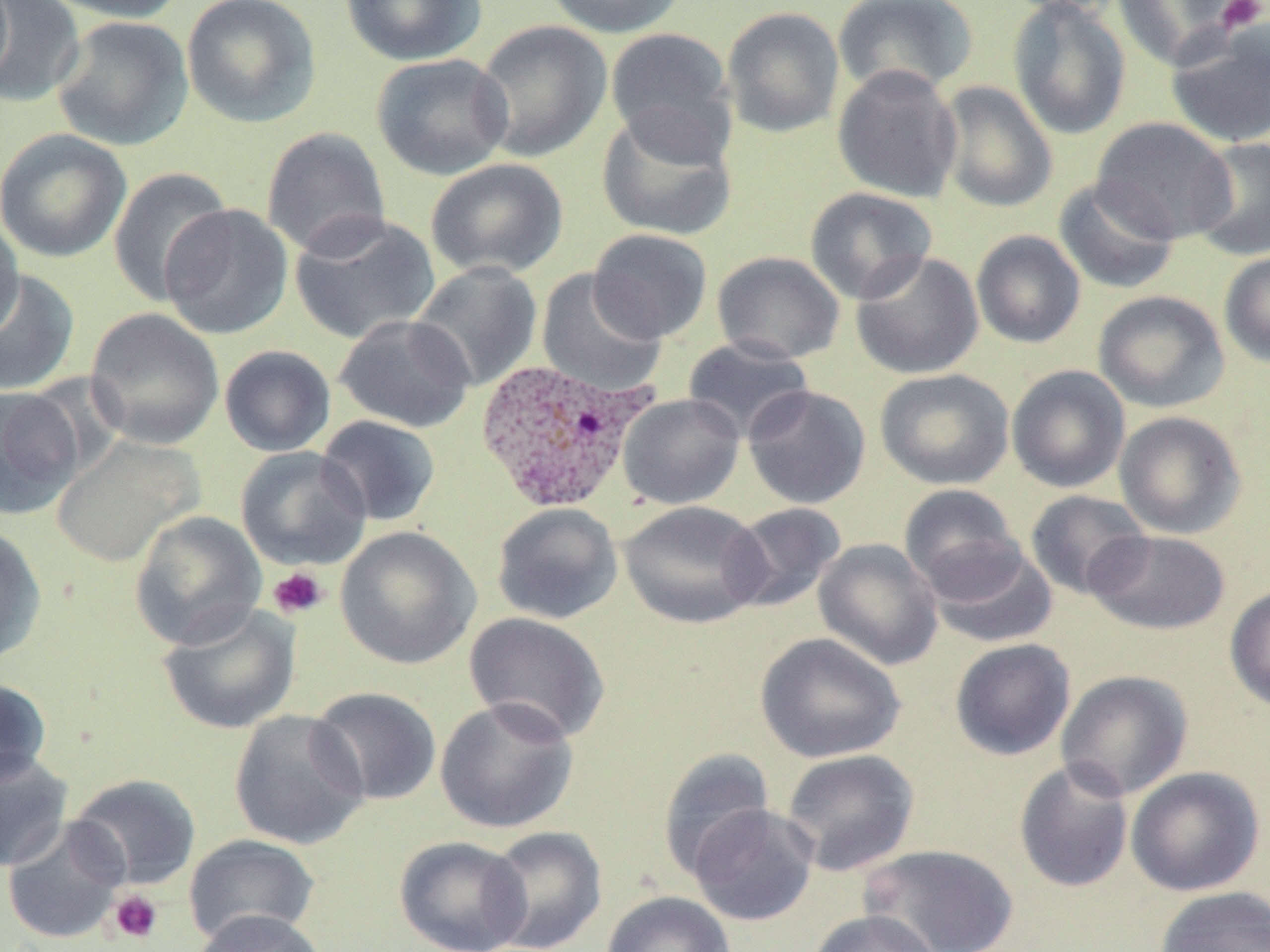
Approximate bounding boxes as [x1, y1, x2, y2] in pixels. Uninfected red blood cell locations: [0, 0, 86, 108], [40, 0, 187, 23], [181, 0, 322, 129], [339, 0, 488, 65], [542, 0, 690, 38], [832, 0, 979, 98], [997, 0, 1126, 17], [1007, 0, 1131, 140], [1111, 0, 1250, 70], [721, 6, 845, 138], [51, 15, 193, 152], [473, 20, 612, 163], [1164, 21, 1270, 149], [605, 26, 737, 161], [371, 52, 512, 180], [832, 64, 963, 203], [936, 81, 1058, 213], [596, 109, 739, 242], [1092, 117, 1238, 244], [261, 126, 391, 260], [0, 128, 132, 263], [1190, 136, 1270, 261], [425, 158, 569, 279], [107, 166, 232, 307], [1053, 177, 1181, 295], [805, 187, 938, 305], [160, 203, 294, 340], [0, 212, 24, 342], [289, 212, 441, 346], [588, 228, 712, 343], [971, 230, 1086, 348], [850, 250, 984, 379], [1218, 250, 1270, 368], [712, 251, 846, 364], [410, 261, 543, 392], [0, 269, 80, 396], [536, 270, 667, 398], [1093, 290, 1229, 413], [85, 308, 224, 450], [333, 313, 476, 433], [682, 336, 814, 443], [219, 345, 336, 457], [1006, 365, 1130, 493], [875, 368, 1014, 490], [0, 385, 84, 518], [742, 385, 872, 509], [618, 393, 745, 509], [1114, 411, 1247, 539], [316, 415, 441, 527], [51, 435, 202, 566], [235, 446, 371, 570], [899, 484, 1024, 598], [1025, 490, 1151, 600], [619, 500, 767, 629], [492, 502, 623, 625], [724, 502, 847, 613], [129, 511, 267, 650], [0, 525, 47, 666], [335, 526, 481, 669], [1085, 529, 1231, 635], [813, 538, 944, 670], [923, 542, 1058, 648], [1224, 584, 1270, 713], [157, 602, 301, 735], [463, 612, 611, 744], [755, 632, 905, 763], [949, 638, 1076, 761], [1055, 670, 1193, 800], [0, 677, 52, 787], [308, 687, 442, 806], [435, 696, 579, 834], [229, 709, 370, 850], [657, 747, 775, 881], [780, 748, 920, 876], [0, 752, 73, 872], [1013, 759, 1135, 893], [1126, 766, 1265, 897], [68, 773, 202, 890], [688, 803, 819, 926], [1, 816, 129, 945], [483, 826, 607, 952], [183, 834, 321, 947], [394, 835, 532, 952], [859, 844, 1020, 952], [1153, 885, 1270, 952], [601, 890, 736, 952], [190, 908, 329, 952], [807, 909, 941, 952]. Plasmodium ovale-infected red blood cell locations: [473, 357, 656, 514]. Platelet locations: [1215, 0, 1268, 34], [267, 567, 329, 619], [107, 889, 163, 944]. Slide-level diagnosis: Plasmodium ovale. 1000x magnification. May-Grünwald-Giemsa stain. Image is 1270×952 pixels. Single field of view. Optical microscopy. Thin blood film.